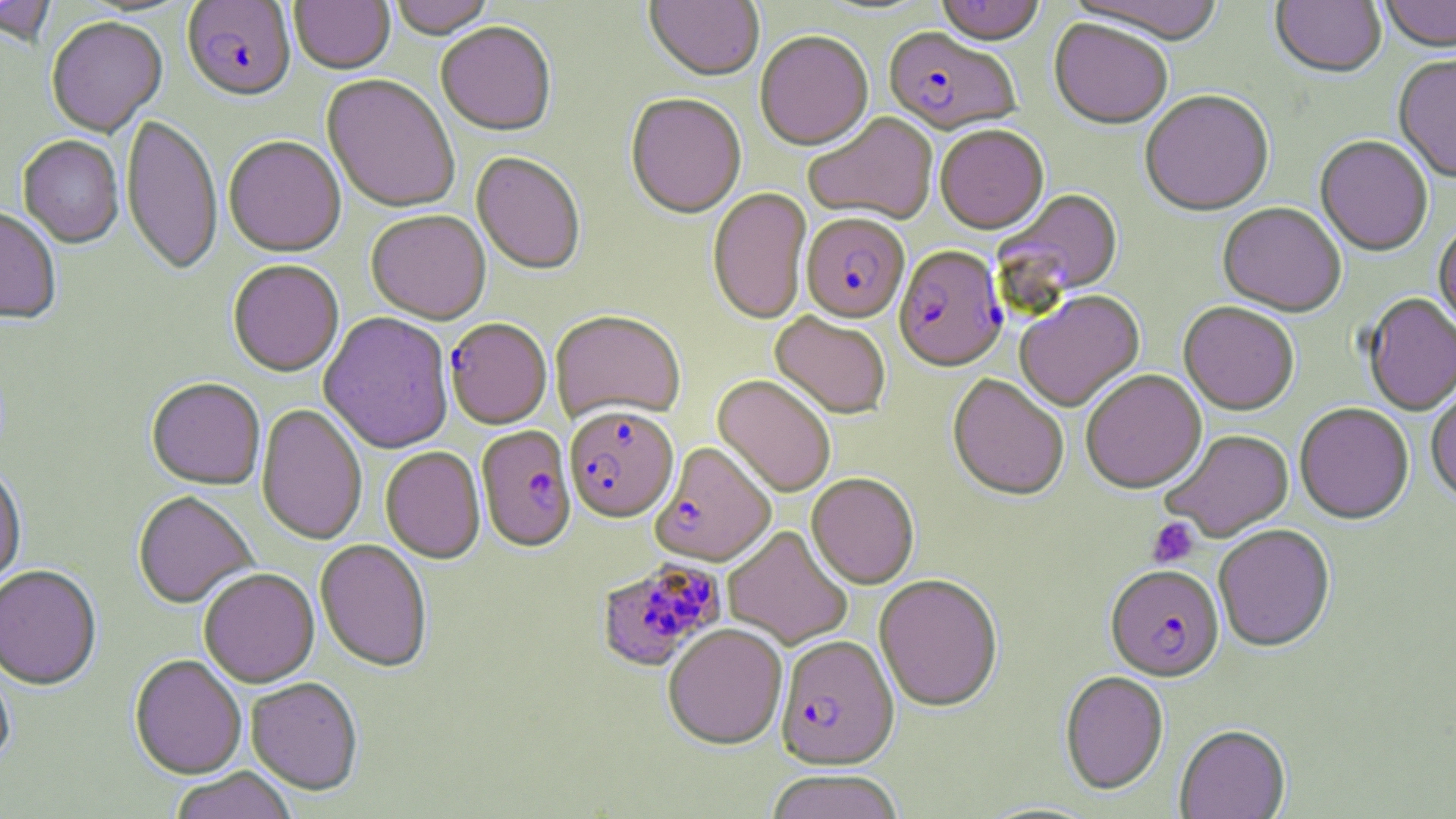
slide-level diagnosis = Plasmodium falciparum
stain = May-Grünwald-Giemsa
preparation = thin blood film
magnification = 1000x
image size = 1456×819 pixels
Plasmodium falciparum-infected red blood cell locations = approximate bounding boxes as (x1, y1, x2, y2) in pixels: (181, 1, 297, 104), (882, 29, 1020, 138), (800, 215, 910, 325), (894, 247, 1008, 374), (445, 318, 552, 431), (565, 407, 679, 525), (476, 426, 576, 554), (651, 443, 775, 568), (595, 557, 727, 673), (1105, 567, 1224, 685), (775, 637, 899, 771)
platelet locations = approximate bounding boxes as (x1, y1, x2, y2) in pixels: (1147, 517, 1199, 568)
field of view = single
modality = light microscopy
uninfected red blood cell locations = approximate bounding boxes as (x1, y1, x2, y2) in pixels: (0, 0, 58, 49), (388, 0, 495, 41), (644, 0, 764, 84), (935, 0, 1045, 48), (1063, 0, 1226, 47), (1379, 0, 1456, 56), (289, 1, 394, 76), (1270, 1, 1386, 81), (46, 18, 167, 139), (1049, 21, 1173, 132), (436, 24, 557, 139), (755, 34, 873, 153), (1394, 57, 1456, 185), (321, 76, 460, 215), (1139, 92, 1275, 219), (625, 95, 746, 221), (804, 113, 939, 226), (121, 114, 223, 279), (935, 127, 1049, 236), (18, 137, 124, 250), (224, 137, 346, 260), (1315, 137, 1433, 259), (470, 153, 585, 277), (707, 189, 812, 326), (995, 189, 1125, 306), (1217, 204, 1346, 319), (0, 209, 61, 325), (366, 212, 491, 326), (1434, 224, 1456, 341), (228, 262, 344, 378), (1015, 291, 1145, 414), (1363, 295, 1456, 416), (1179, 303, 1298, 417), (550, 312, 685, 425), (318, 313, 454, 455), (770, 313, 891, 420), (1081, 372, 1207, 496), (948, 374, 1069, 503), (712, 375, 836, 497), (146, 379, 265, 491), (1426, 390, 1456, 506), (256, 404, 368, 547), (1295, 404, 1413, 527), (1162, 431, 1295, 544), (380, 447, 485, 565), (0, 466, 27, 596), (807, 474, 919, 590), (133, 492, 257, 610), (723, 525, 853, 650), (1214, 526, 1336, 655), (315, 540, 432, 674), (0, 566, 102, 693), (198, 570, 319, 689), (873, 575, 1003, 714), (662, 625, 787, 751), (0, 654, 15, 773), (129, 656, 247, 781), (1060, 672, 1168, 797), (245, 679, 363, 798), (1174, 727, 1291, 819), (169, 769, 297, 819), (767, 771, 905, 819)